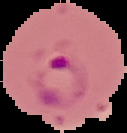
result = malaria parasites identified
preparation = thin blood smear
image size = 127×133 pixels
image type = segmented cell region on a black background